Identify the parasite.
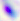

This is Toxoplasma gondii.

Summary:
  - Magnification: 400x
  - Modality: micrograph